Give the position of every malaria parasite.
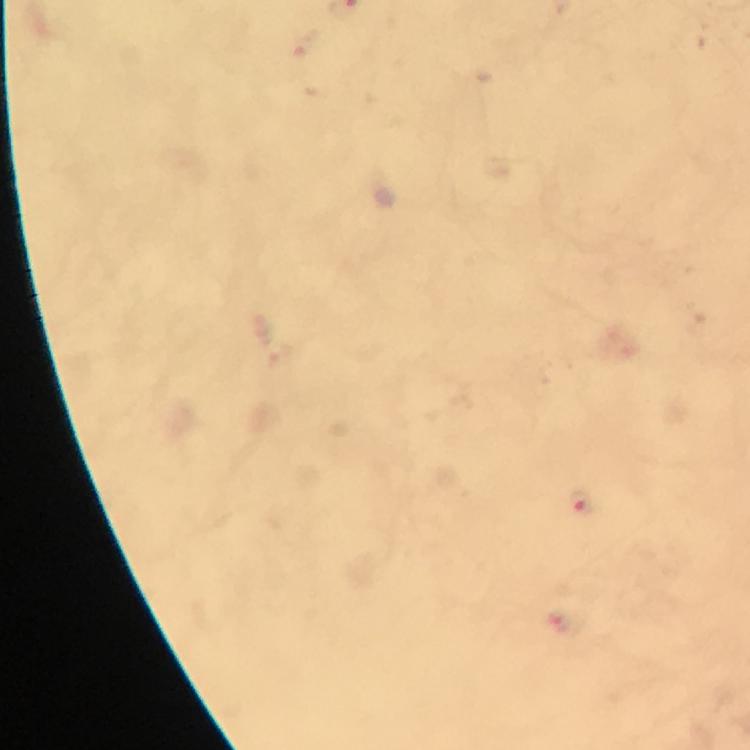
Approximate object centers, in pixels from the top-left corner.
Malaria parasites: (x=579, y=503).

Summary:
  - Immersion oil: used
  - Magnification: 100x
  - Capture: smartphone camera through the microscope
  - Cropped from: a single field of view
  - Context: from a malaria diagnostic workup
  - Image size: 750×750 pixels
  - Preparation: thick blood film
  - Stain: Giemsa